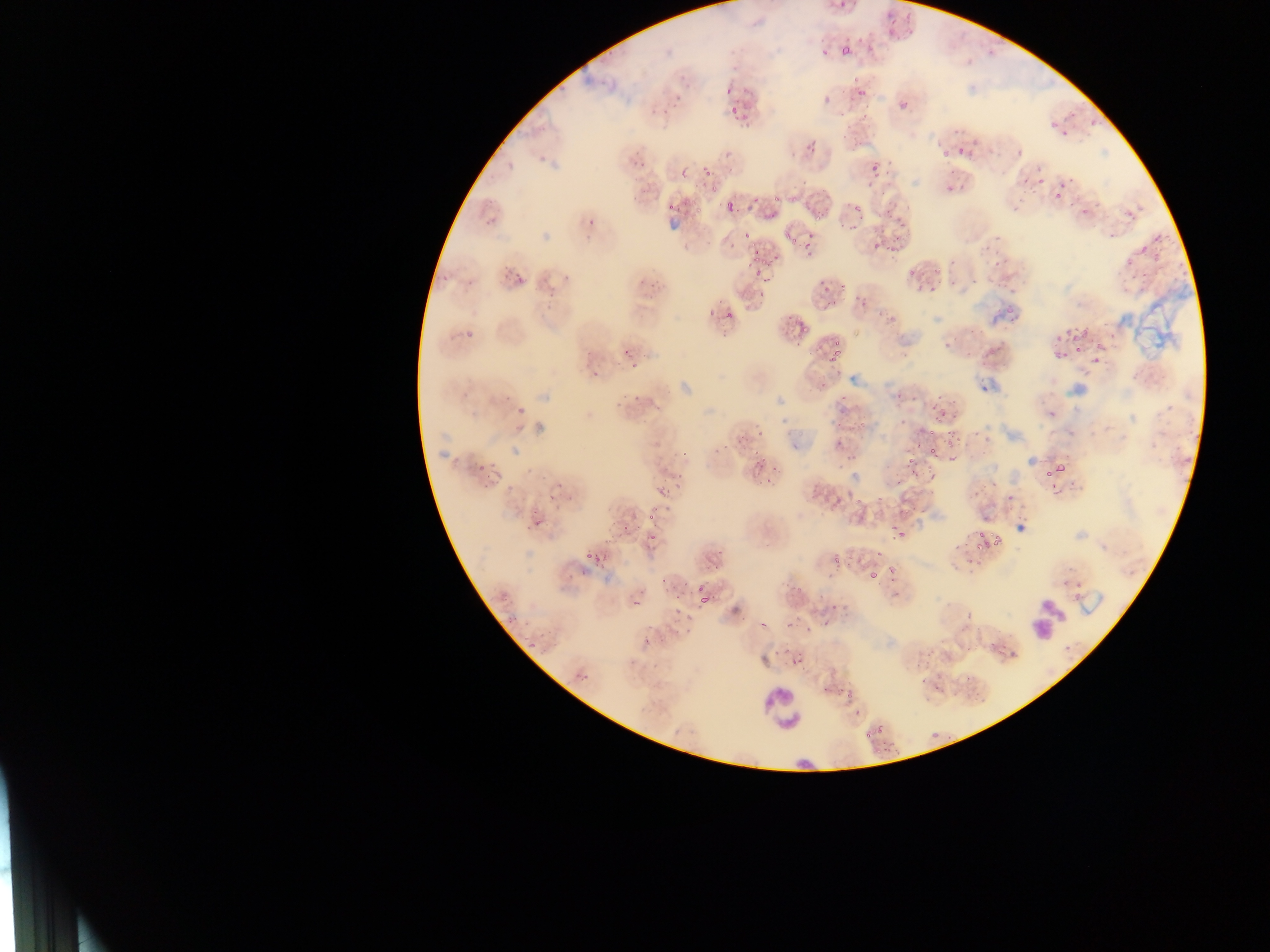

Plasmodium parasite locations = approximate bounding boxes as {left, top, right, bottom} in pixels: {836, 0, 851, 11}, {888, 5, 903, 23}, {902, 19, 919, 32}, {888, 28, 896, 35}, {857, 30, 864, 43}, {842, 35, 855, 48}, {865, 40, 874, 52}, {840, 46, 853, 55}, {821, 47, 829, 59}, {850, 76, 860, 83}, {722, 85, 736, 97}, {855, 87, 868, 96}, {672, 91, 689, 101}, {899, 102, 906, 110}, {728, 106, 741, 116}, {858, 106, 872, 122}, {1065, 109, 1081, 120}, {732, 115, 749, 126}, {1087, 118, 1098, 131}, {1049, 120, 1059, 129}, {951, 127, 967, 135}, {1061, 129, 1074, 140}, {850, 132, 864, 152}, {804, 136, 821, 154}, {953, 143, 969, 154}, {1016, 148, 1026, 160}, {938, 149, 951, 158}, {628, 152, 647, 161}, {886, 157, 894, 166}, {883, 161, 893, 179}, {869, 164, 885, 181}, {677, 166, 691, 178}, {701, 166, 711, 176}, {1037, 166, 1043, 175}, {1063, 171, 1077, 183}, {1022, 173, 1032, 190}, {1033, 174, 1048, 187}, {708, 177, 723, 195}, {862, 181, 871, 190}, {943, 181, 952, 193}, {1055, 185, 1066, 204}, {1030, 188, 1037, 197}, {772, 189, 782, 204}, {787, 195, 798, 205}, {718, 197, 740, 212}, {751, 197, 760, 206}, {692, 198, 707, 214}, {482, 200, 506, 224}, {668, 200, 679, 213}, {883, 200, 895, 216}, {850, 204, 864, 215}, {1012, 204, 1021, 213}, {1080, 204, 1092, 218}, {898, 207, 910, 224}, {1126, 208, 1137, 220}, {766, 210, 777, 221}, {583, 213, 602, 224}, {813, 213, 824, 224}, {844, 220, 861, 232}, {784, 223, 808, 246}, {744, 224, 756, 240}, {1109, 229, 1120, 240}, {805, 230, 819, 261}, {870, 236, 883, 253}, {990, 236, 1000, 243}, {728, 237, 737, 248}, {887, 238, 899, 255}, {981, 241, 993, 254}, {753, 250, 763, 258}, {512, 252, 536, 285}, {1128, 254, 1141, 265}, {746, 255, 760, 269}, {992, 255, 1007, 267}, {770, 257, 780, 269}, {949, 259, 963, 272}, {933, 266, 949, 272}, {908, 269, 918, 278}, {1142, 269, 1151, 278}, {438, 270, 452, 280}, {754, 270, 765, 278}, {1132, 272, 1138, 281}, {762, 276, 773, 286}, {951, 276, 957, 284}, {971, 276, 979, 288}, {635, 277, 644, 285}, {911, 278, 927, 292}, {993, 280, 1004, 289}, {929, 282, 939, 295}, {544, 283, 556, 296}, {648, 283, 663, 289}, {822, 283, 832, 292}, {838, 283, 852, 294}, {1137, 283, 1147, 295}, {1003, 284, 1016, 297}, {1121, 286, 1129, 296}, {645, 293, 659, 310}, {724, 303, 740, 322}, {1007, 308, 1016, 314}, {708, 311, 718, 320}, {461, 317, 484, 343}, {797, 324, 811, 337}, {967, 327, 982, 336}, {1051, 327, 1060, 342}, {1107, 327, 1117, 344}, {1068, 329, 1086, 340}, {1090, 330, 1108, 366}, {835, 334, 842, 351}, {941, 336, 955, 351}, {614, 343, 635, 363}, {793, 343, 804, 348}, {982, 343, 999, 358}, {1073, 343, 1089, 354}, {828, 344, 847, 365}, {1050, 344, 1067, 360}, {966, 347, 976, 363}, {629, 360, 640, 369}, {590, 370, 600, 379}, {820, 379, 830, 390}, {632, 390, 649, 402}, {934, 392, 960, 418}, {610, 393, 625, 408}, {506, 394, 515, 400}, {840, 394, 846, 403}, {1162, 401, 1173, 415}, {931, 404, 947, 423}, {519, 406, 528, 415}, {1045, 406, 1060, 423}, {753, 410, 764, 444}, {853, 419, 868, 429}, {835, 420, 843, 430}, {926, 428, 939, 436}, {971, 429, 980, 445}, {1188, 429, 1199, 439}, {945, 433, 958, 450}, {736, 436, 750, 450}, {833, 439, 845, 445}, {714, 440, 733, 455}, {678, 445, 690, 456}, {929, 449, 938, 456}, {1181, 451, 1193, 466}, {846, 452, 858, 463}, {946, 452, 958, 466}, {751, 455, 770, 473}, {905, 458, 915, 470}, {472, 459, 488, 470}, {1042, 461, 1067, 480}, {925, 466, 937, 481}, {909, 467, 920, 477}, {762, 470, 778, 487}, {676, 472, 688, 489}, {483, 473, 492, 487}, {984, 473, 1000, 491}, {660, 475, 668, 482}, {1045, 480, 1066, 495}, {550, 481, 570, 489}, {1006, 484, 1022, 501}, {971, 487, 982, 501}, {654, 488, 670, 499}, {546, 492, 558, 500}, {856, 494, 864, 508}, {876, 496, 885, 504}, {832, 499, 843, 509}, {645, 503, 658, 522}, {535, 514, 544, 529}, {619, 514, 634, 534}, {894, 521, 911, 538}, {524, 526, 532, 532}, {650, 530, 664, 545}, {990, 530, 1002, 552}, {963, 531, 974, 543}, {979, 531, 986, 546}, {577, 532, 601, 561}, {974, 538, 984, 553}, {950, 541, 959, 550}, {715, 547, 727, 559}, {873, 549, 883, 561}, {829, 555, 842, 569}, {594, 556, 607, 572}, {887, 557, 907, 575}, {964, 557, 982, 567}, {867, 562, 887, 585}, {710, 565, 721, 574}, {580, 567, 588, 576}, {1062, 573, 1086, 599}, {659, 574, 675, 586}, {567, 575, 575, 579}, {788, 578, 807, 593}, {671, 582, 688, 604}, {697, 582, 706, 593}, {890, 586, 901, 601}, {500, 591, 512, 602}, {698, 594, 710, 605}, {632, 596, 649, 609}, {829, 600, 838, 614}, {670, 606, 684, 615}, {963, 610, 973, 624}, {683, 612, 694, 624}, {758, 614, 773, 629}, {507, 616, 518, 624}, {684, 617, 696, 637}, {784, 618, 794, 627}, {671, 620, 680, 630}, {820, 621, 828, 628}, {803, 624, 813, 633}, {992, 624, 1007, 650}, {528, 637, 542, 649}, {642, 637, 653, 647}, {995, 646, 1007, 663}, {783, 647, 792, 657}, {789, 647, 809, 666}, {968, 647, 979, 669}, {575, 667, 593, 681}, {916, 669, 931, 686}, {964, 673, 971, 683}, {819, 682, 831, 693}, {934, 684, 941, 693}, {843, 689, 855, 702}, {854, 708, 863, 716}, {876, 722, 885, 739}, {864, 727, 873, 742}, {932, 727, 941, 744}, {871, 747, 885, 758} | approximate {x, y} pixel centers of objects too small to bound: {650, 627}, {776, 652}
capture = mobile-phone photograph through a microscope
field of view = single
leukocyte locations = approximate bounding boxes as {left, top, right, bottom} in pixels: {1026, 590, 1065, 649}, {760, 687, 807, 733}
country = Ghana
preparation = thin blood smear
image size = 1270×952 pixels